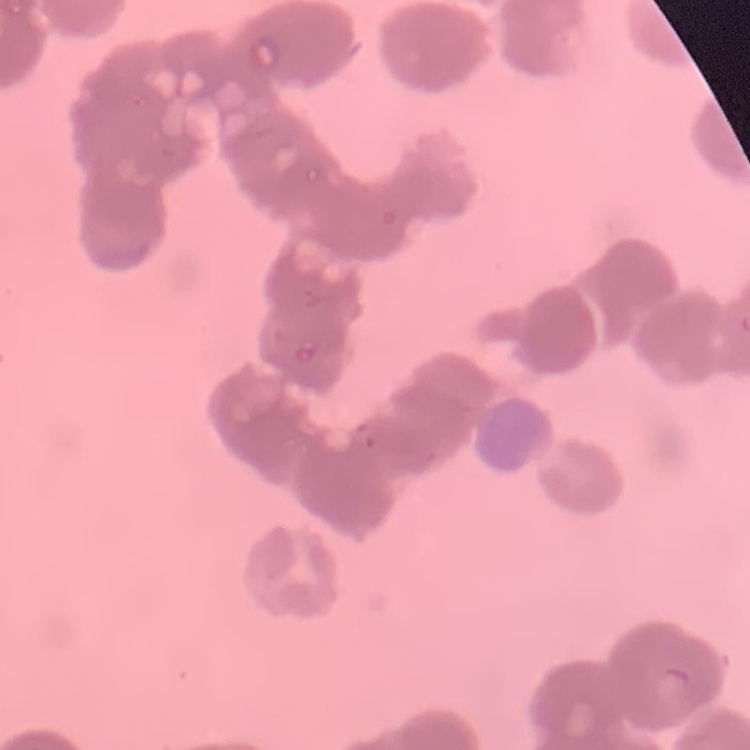

Summary:
  - Red blood cell morphology: rouleaux formation
  - Image type: one tile cut from a larger photomicrograph
  - Preparation: thin blood smear
  - Stain: Field's or Giemsa